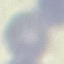
Summary:
  - Malaria status: uninfected
  - Image type: automatically extracted cell patch, resized to 64 × 64 pixels
  - Preparation: thin smear
  - Stain: Giemsa
  - Capture: smartphone through the microscope eyepiece